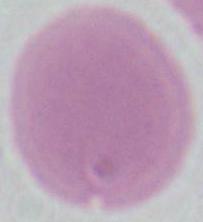

An erythrocyte is seen. 1000x magnification. Photomicrograph.